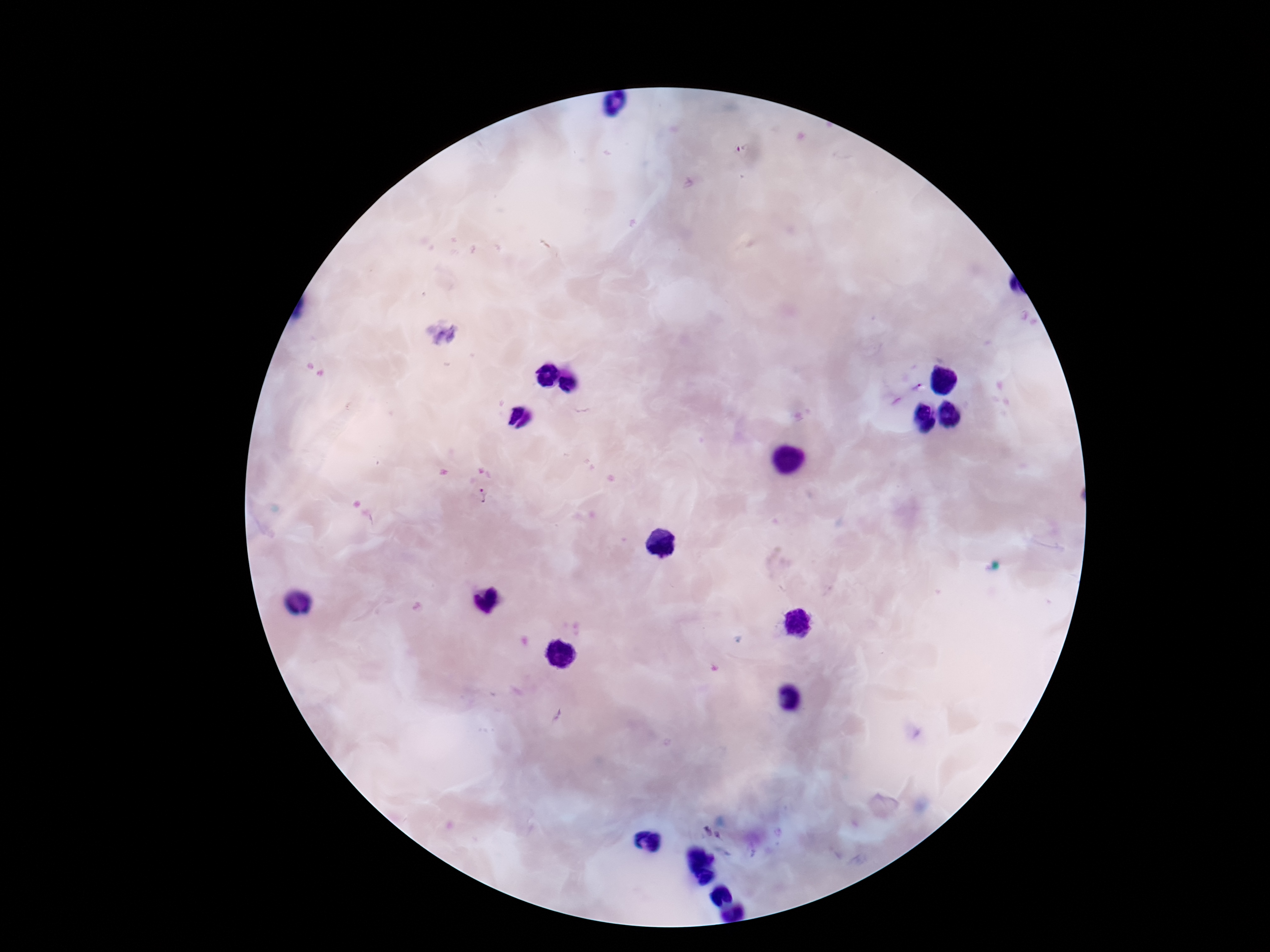

Approximate object centers, in pixels from the top-left corner. Plasmodium parasite locations: (x=916, y=387), (x=481, y=496). Smartphone photograph taken through the microscope eyepiece. Patient malaria status: infected. 100x magnification. One field from this slide. Giemsa stain. Thick blood film. Image is 1270×952 pixels.